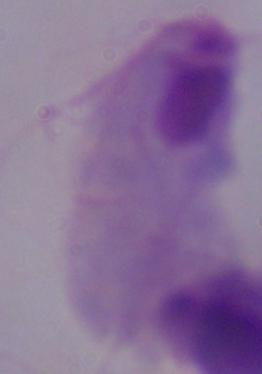 Micrograph. 1000x magnification. A trichomonad is seen.